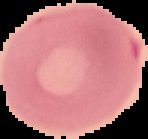
{
  "preparation": "thin blood smear",
  "image_size": "148×139 pixels",
  "result": "no malaria parasites detected",
  "image_type": "segmented cell region on a black background"
}